Assess this cell for malaria.
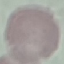
Uninfected.

Summary:
  - Stain: Giemsa
  - Capture: smartphone through the microscope eyepiece
  - Image type: automatically extracted cell patch, resized to 64 × 64 pixels
  - Preparation: thin smear